Give the position of every leukocyte visible.
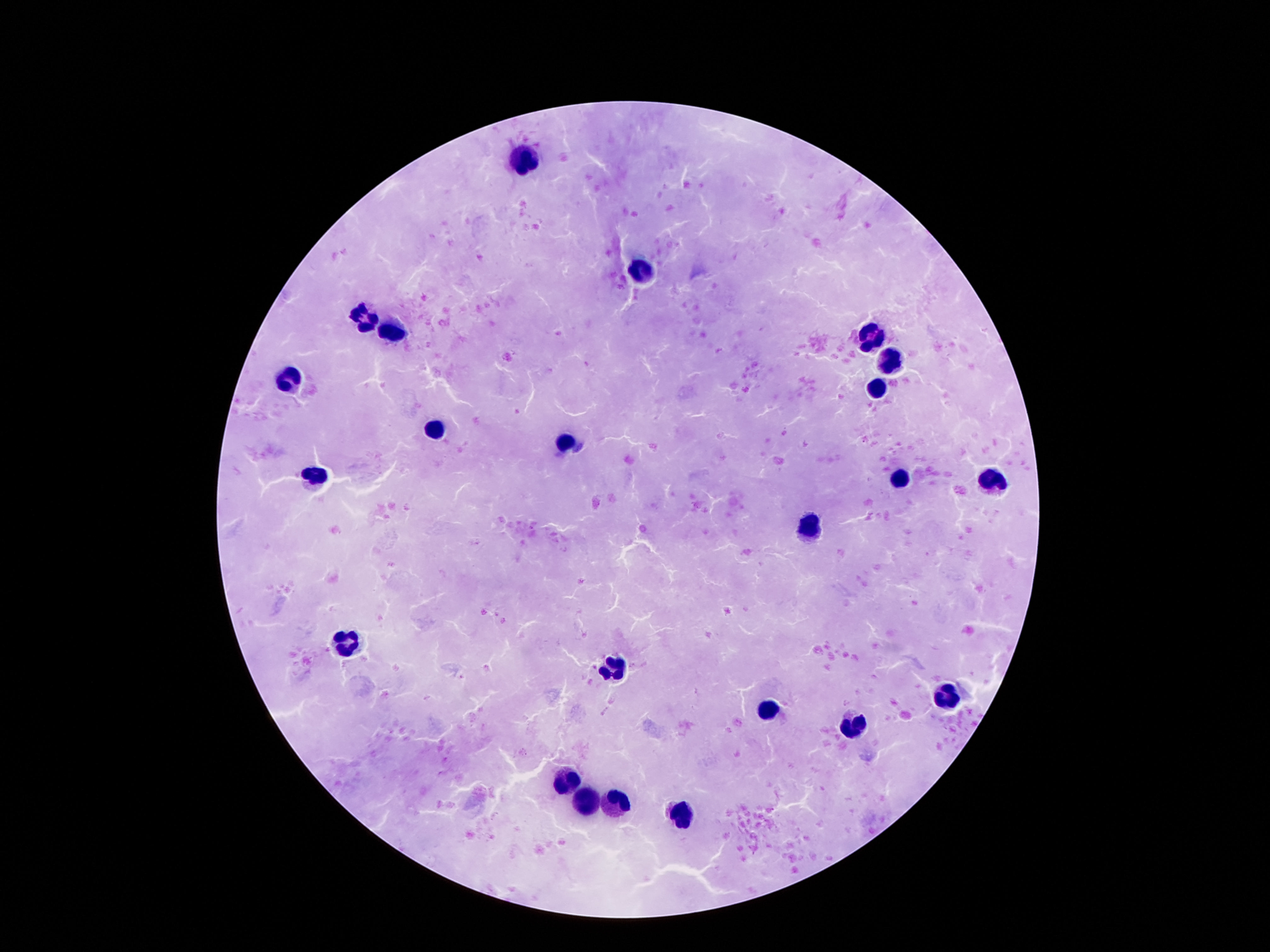

Approximate object centers, in pixels from the top-left corner.
Leukocytes: (x=522, y=160), (x=643, y=270), (x=360, y=318), (x=389, y=331), (x=875, y=338), (x=885, y=359), (x=288, y=379), (x=879, y=387), (x=434, y=430), (x=561, y=442), (x=313, y=477), (x=897, y=479), (x=992, y=485), (x=807, y=529), (x=342, y=644), (x=616, y=671), (x=944, y=697), (x=768, y=709), (x=854, y=730), (x=563, y=781), (x=584, y=800), (x=612, y=803), (x=682, y=818).

{
  "preparation": "thick blood film",
  "capture": "smartphone camera through the microscope eyepiece",
  "patient_malaria_status": "negative",
  "stain": "Giemsa",
  "magnification": "100x",
  "image_size": "1270×952 pixels",
  "field_of_view": "one from this slide"
}